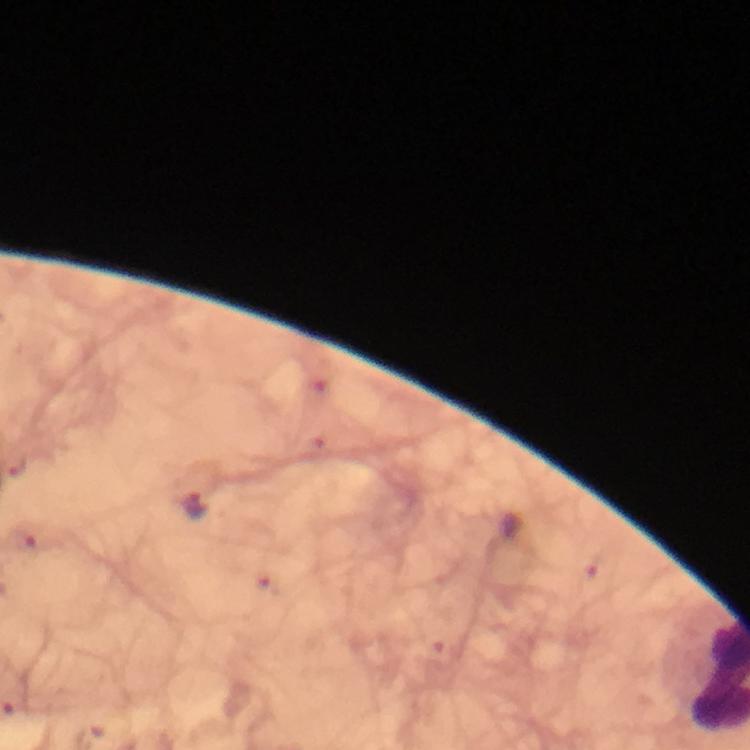
Approximate centers as (x, y) in pixels.
Summary:
  - Plasmodium parasite locations: (193, 507)
  - Cropped from: a single field of view
  - Magnification: 100x
  - Stain: Giemsa
  - Preparation: thick blood smear
  - Image size: 750×750 pixels
  - Context: from a diagnostic examination for malaria
  - Immersion oil: applied
  - Capture: smartphone mounted on the microscope